Describe the morphology of the red blood cells.
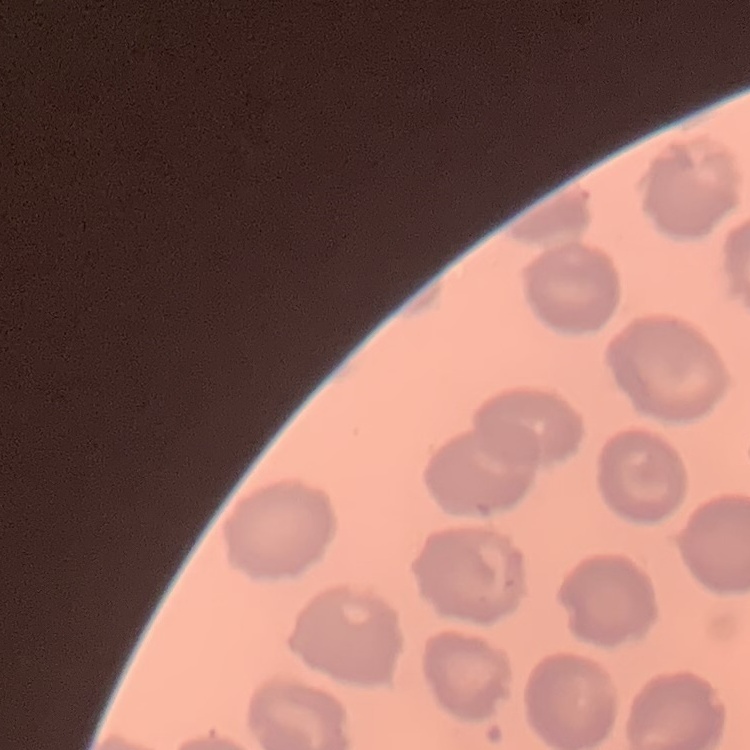

They show no rouleaux formation.

preparation = thin peripheral smear
stain = Field's or Giemsa
image type = square crop of a larger photomicrograph